Assess this cell for malaria.
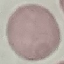
Uninfected.

stain = Giemsa
capture = smartphone through the microscope eyepiece
preparation = thin smear
image type = automatically extracted cell patch, resized to 64 × 64 pixels